Outline each Plasmodium falciparum-infected red blood cell.
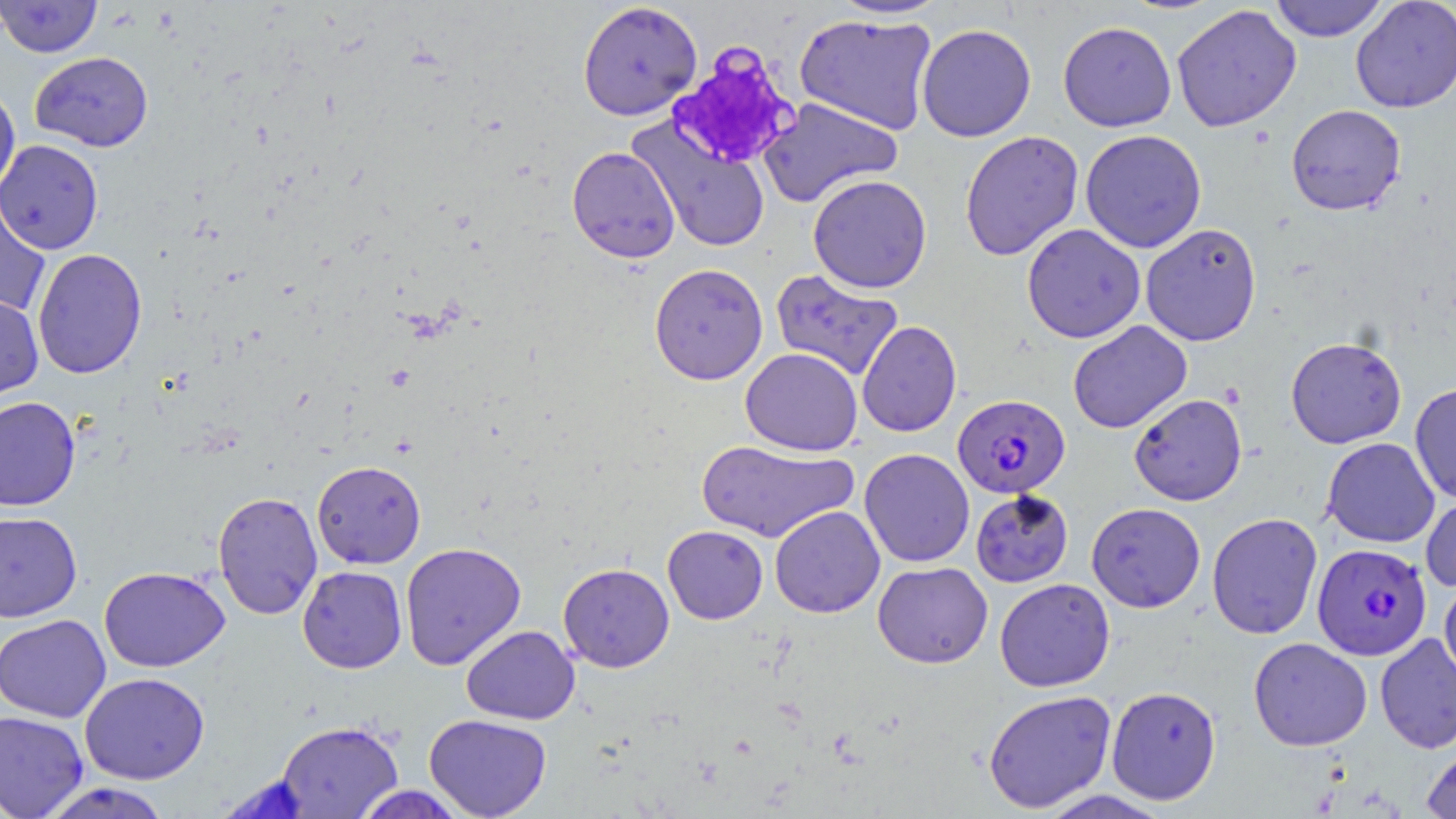

Approximate bounding boxes as named x1/y1/x2/y2 corners in pixels.
Plasmodium falciparum-infected red blood cells: (x1=953, y1=394, x2=1070, y2=498), (x1=1312, y1=543, x2=1432, y2=660).

Summary:
  - Uninfected red blood cell locations: (x1=1, y1=0, x2=103, y2=58), (x1=1269, y1=0, x2=1389, y2=42), (x1=1350, y1=0, x2=1456, y2=113), (x1=577, y1=1, x2=703, y2=121), (x1=831, y1=1, x2=950, y2=21), (x1=1171, y1=4, x2=1302, y2=132), (x1=795, y1=13, x2=938, y2=135), (x1=1058, y1=21, x2=1176, y2=132), (x1=916, y1=23, x2=1036, y2=142), (x1=30, y1=51, x2=153, y2=151), (x1=0, y1=85, x2=20, y2=198), (x1=758, y1=97, x2=903, y2=208), (x1=1286, y1=104, x2=1407, y2=216), (x1=629, y1=118, x2=771, y2=253), (x1=1079, y1=129, x2=1207, y2=253), (x1=960, y1=130, x2=1083, y2=261), (x1=0, y1=139, x2=104, y2=255), (x1=567, y1=146, x2=680, y2=263), (x1=808, y1=174, x2=932, y2=293), (x1=0, y1=193, x2=51, y2=318), (x1=1140, y1=223, x2=1262, y2=346), (x1=1022, y1=224, x2=1146, y2=343), (x1=32, y1=248, x2=147, y2=379), (x1=649, y1=263, x2=768, y2=385), (x1=770, y1=268, x2=903, y2=382), (x1=0, y1=293, x2=43, y2=402), (x1=857, y1=320, x2=961, y2=437), (x1=1068, y1=321, x2=1192, y2=434), (x1=1285, y1=337, x2=1407, y2=448), (x1=740, y1=348, x2=863, y2=456), (x1=1409, y1=383, x2=1456, y2=503), (x1=1129, y1=393, x2=1247, y2=506), (x1=0, y1=396, x2=81, y2=511), (x1=1322, y1=437, x2=1439, y2=547), (x1=697, y1=439, x2=858, y2=543), (x1=859, y1=448, x2=975, y2=567), (x1=311, y1=460, x2=426, y2=569), (x1=970, y1=490, x2=1073, y2=587), (x1=212, y1=491, x2=323, y2=620), (x1=1421, y1=492, x2=1456, y2=593), (x1=1086, y1=502, x2=1205, y2=612), (x1=770, y1=505, x2=885, y2=618), (x1=0, y1=511, x2=83, y2=623), (x1=1207, y1=512, x2=1323, y2=640), (x1=663, y1=525, x2=768, y2=624), (x1=400, y1=542, x2=526, y2=670), (x1=873, y1=561, x2=993, y2=669), (x1=558, y1=562, x2=674, y2=672), (x1=99, y1=566, x2=230, y2=672), (x1=297, y1=566, x2=407, y2=673), (x1=995, y1=578, x2=1115, y2=692), (x1=1439, y1=578, x2=1456, y2=686), (x1=0, y1=614, x2=111, y2=723), (x1=461, y1=625, x2=580, y2=725), (x1=1375, y1=632, x2=1456, y2=754), (x1=1248, y1=637, x2=1372, y2=751), (x1=79, y1=672, x2=209, y2=784), (x1=1106, y1=685, x2=1221, y2=805), (x1=983, y1=690, x2=1117, y2=813), (x1=0, y1=710, x2=89, y2=819), (x1=424, y1=713, x2=552, y2=818), (x1=276, y1=720, x2=403, y2=818), (x1=1421, y1=741, x2=1456, y2=819), (x1=216, y1=775, x2=313, y2=818), (x1=38, y1=782, x2=174, y2=819), (x1=350, y1=785, x2=470, y2=819), (x1=1034, y1=789, x2=1174, y2=819)
  - Platelet locations: (x1=667, y1=42, x2=801, y2=169)
  - Slide-level diagnosis: Plasmodium falciparum
  - Image size: 1456×819 pixels
  - Magnification: 1000x
  - Modality: optical microscopy
  - Preparation: thin blood smear
  - Field of view: single
  - Stain: May-Grünwald-Giemsa